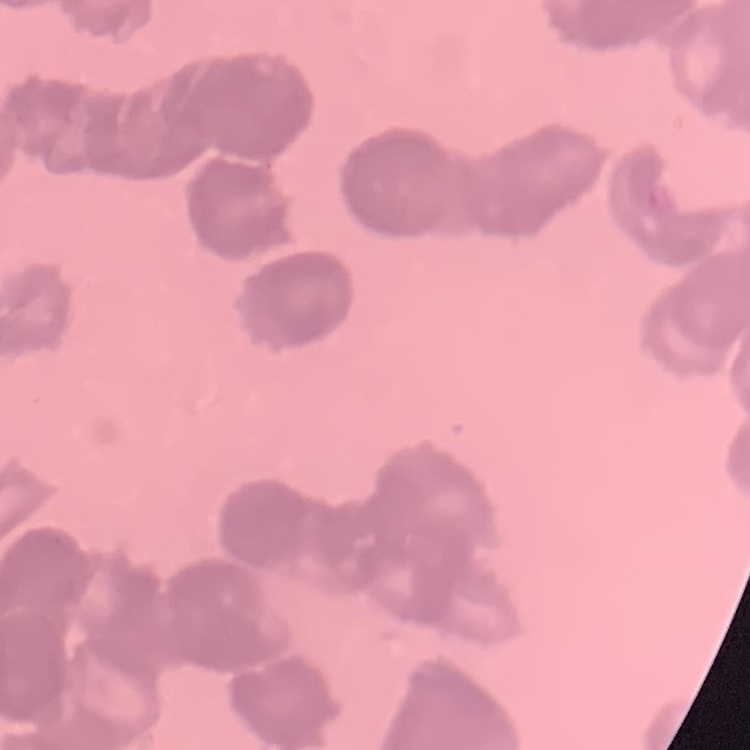 The erythrocytes show rouleaux formation. Thin peripheral smear. Stained with either Field's or Giemsa. One tile cut from a larger photomicrograph.